Outline each Plasmodium ovale-infected red blood cell.
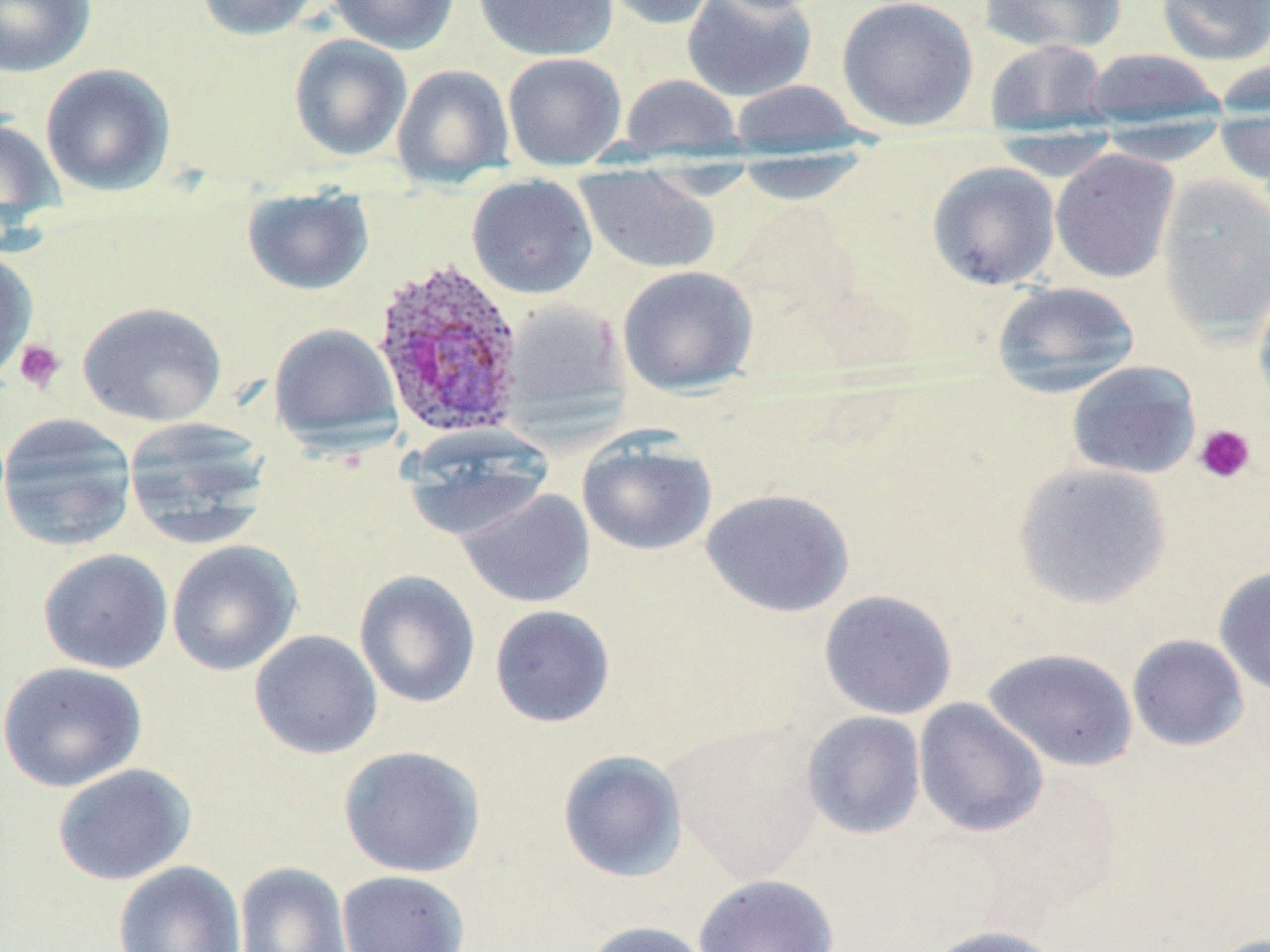
Approximate bounding boxes as (x1, y1, x2, y2) in pixels.
Plasmodium ovale-infected red blood cells: (371, 258, 525, 439).

slide-level diagnosis = Plasmodium ovale
stain = May-Grünwald-Giemsa
platelet locations = approximate bounding boxes as (x1, y1, x2, y2) in pixels: (13, 338, 66, 393), (1193, 424, 1256, 485)
magnification = 1000x
image size = 1270×952 pixels
field of view = one of a larger specimen
modality = light microscopy
uninfected red blood cell locations = approximate bounding boxes as (x1, y1, x2, y2) in pixels: (0, 0, 96, 78), (195, 0, 322, 41), (329, 0, 459, 54), (473, 0, 617, 61), (596, 0, 721, 31), (681, 0, 817, 102), (836, 0, 979, 132), (978, 0, 1127, 54), (1156, 0, 1270, 65), (288, 34, 413, 161), (985, 38, 1111, 134), (1082, 48, 1225, 127), (502, 52, 627, 169), (1210, 58, 1270, 117), (40, 63, 177, 197), (392, 65, 514, 186), (619, 73, 743, 160), (729, 79, 865, 153), (1212, 112, 1270, 190), (0, 117, 65, 230), (1093, 117, 1233, 165), (985, 128, 1122, 181), (1050, 149, 1180, 283), (729, 152, 871, 206), (926, 161, 1061, 290), (574, 167, 721, 275), (465, 173, 598, 299), (1156, 175, 1270, 342), (241, 189, 374, 296), (0, 251, 38, 382), (617, 265, 759, 395), (1254, 275, 1270, 416), (992, 281, 1141, 397), (499, 298, 632, 433), (77, 301, 227, 427), (268, 322, 402, 449), (1065, 361, 1201, 480), (0, 413, 138, 552), (122, 417, 274, 548), (400, 427, 554, 542), (577, 435, 717, 556), (1011, 462, 1173, 610), (456, 488, 595, 608), (700, 488, 855, 618), (166, 540, 302, 676), (37, 549, 174, 674), (1213, 565, 1270, 697), (354, 569, 481, 708), (818, 589, 957, 720), (489, 605, 616, 728), (249, 629, 383, 759), (1126, 634, 1249, 752), (982, 647, 1139, 772), (1, 661, 147, 793), (914, 698, 1048, 837), (801, 711, 926, 840), (665, 720, 824, 883), (338, 745, 485, 877), (557, 749, 688, 882), (52, 763, 196, 886), (113, 860, 246, 952), (234, 861, 353, 952), (336, 870, 470, 952), (693, 874, 840, 952), (582, 920, 715, 952), (923, 924, 1066, 952)
preparation = thin blood smear